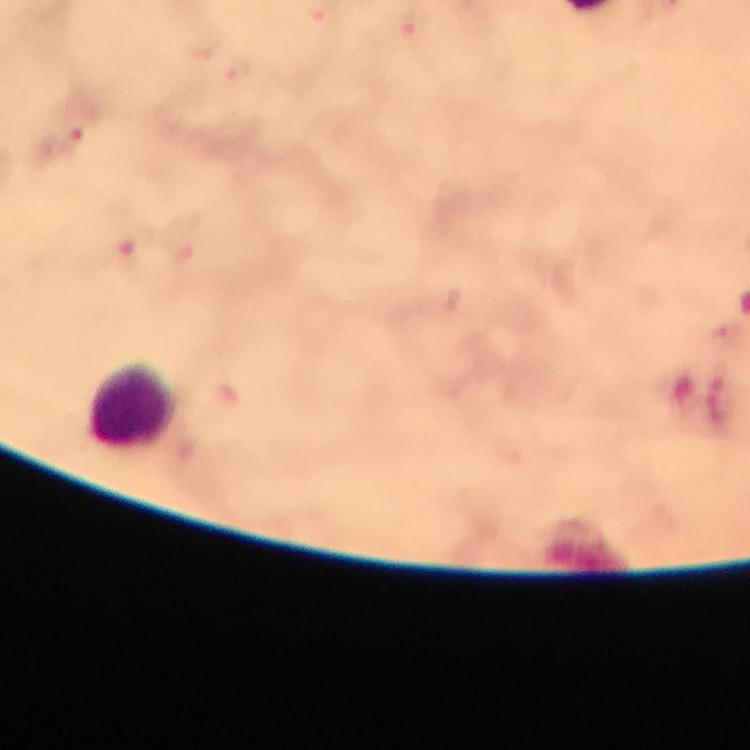 Approximate centers as {x, y} in pixels. Leukocyte locations: {134, 406}. Plasmodium parasite locations: {411, 27}, {239, 75}, {64, 147}, {451, 299}. Smartphone photograph taken through a microscope. At 100x magnification. Giemsa stain. Thick blood smear. Image is 750×750 pixels. From a malaria diagnostic workup. Cropped region of a single field of view. Immersion oil was used.